Report the malaria status of this cell.
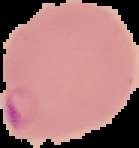

It is parasitized.

image size = 139×148 pixels
preparation = thin blood film
image type = segmented cell region with the area outside set to black